Comment on the morphology of the erythrocytes.
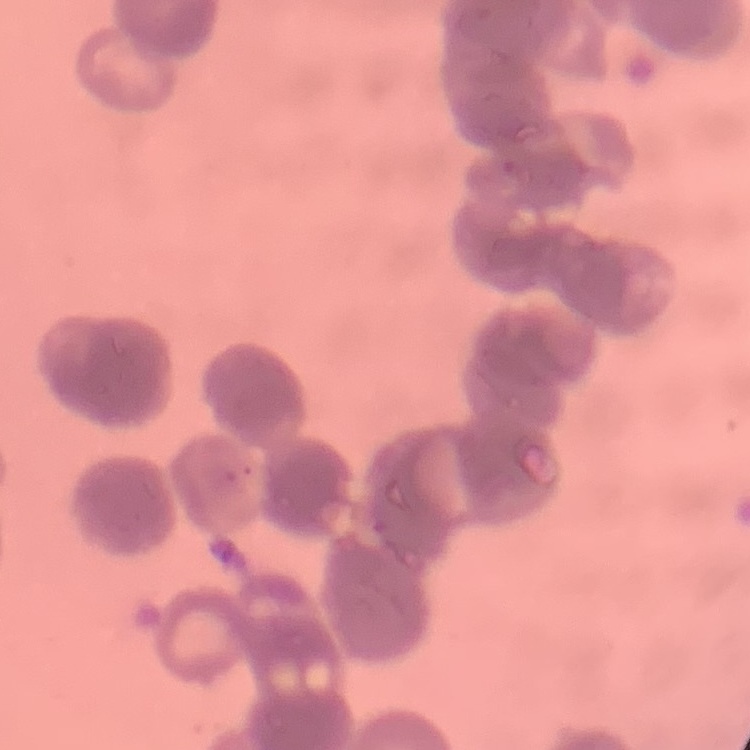

They show rouleaux formation.

Thin blood smear. Field's or Giemsa stain. Square crop of a larger photomicrograph.